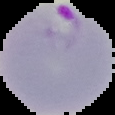

image type = cell region segmented out of the field of view; surrounding area masked to black
image size = 115×115 pixels
result = malaria parasites identified
preparation = thin blood film